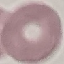

Summary:
  - Malaria status: uninfected
  - Preparation: thin smear
  - Stain: Giemsa
  - Capture: smartphone camera at the microscope eyepiece
  - Image type: automatically extracted cell patch, resized to 64 × 64 pixels